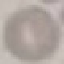
Summary:
  - Malaria status: uninfected
  - Stain: Giemsa
  - Image type: automatically extracted cell patch, resized to 64 × 64 pixels
  - Preparation: thin blood film
  - Capture: smartphone through the microscope eyepiece